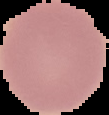
Summary:
  - Image size: 109×115 pixels
  - Preparation: thin blood film
  - Image type: segmented cell region with the area outside set to black
  - Result: no malaria parasites seen